Report the malaria status.
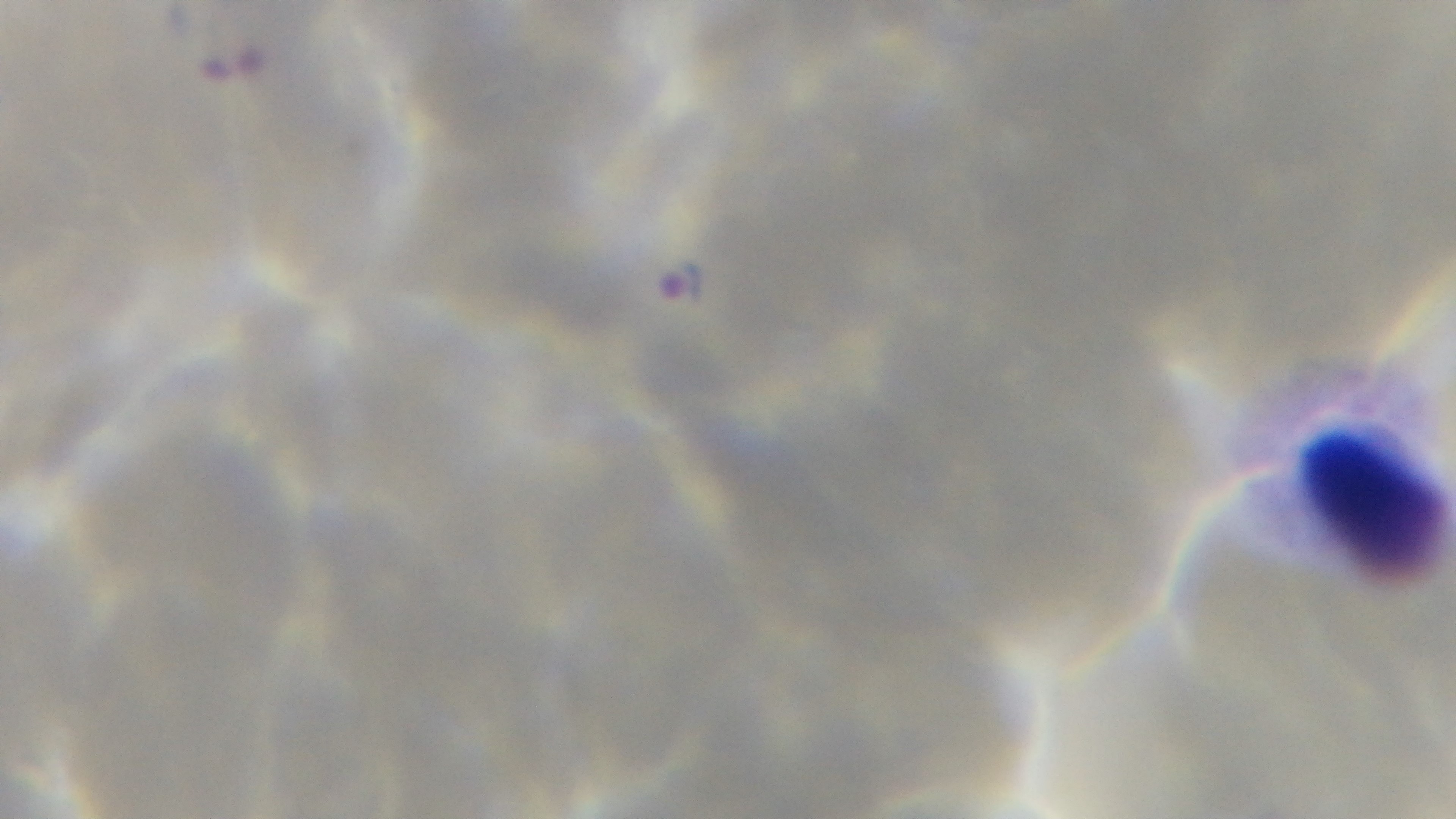

It is infected.

Summary:
  - Stain: Giemsa
  - Modality: light microscopy
  - Preparation: thin
  - Capture: mounted 4K digital camera
  - Field of view: single
  - Objective: 100x oil immersion